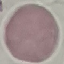

Malaria status: uninfected. Giemsa-stained preparation. Automatically extracted cell patch, resized to 64 × 64 pixels. Acquired by smartphone through the microscope eyepiece. Thin smear of blood.